Give the position of every Plasmodium parasite visible.
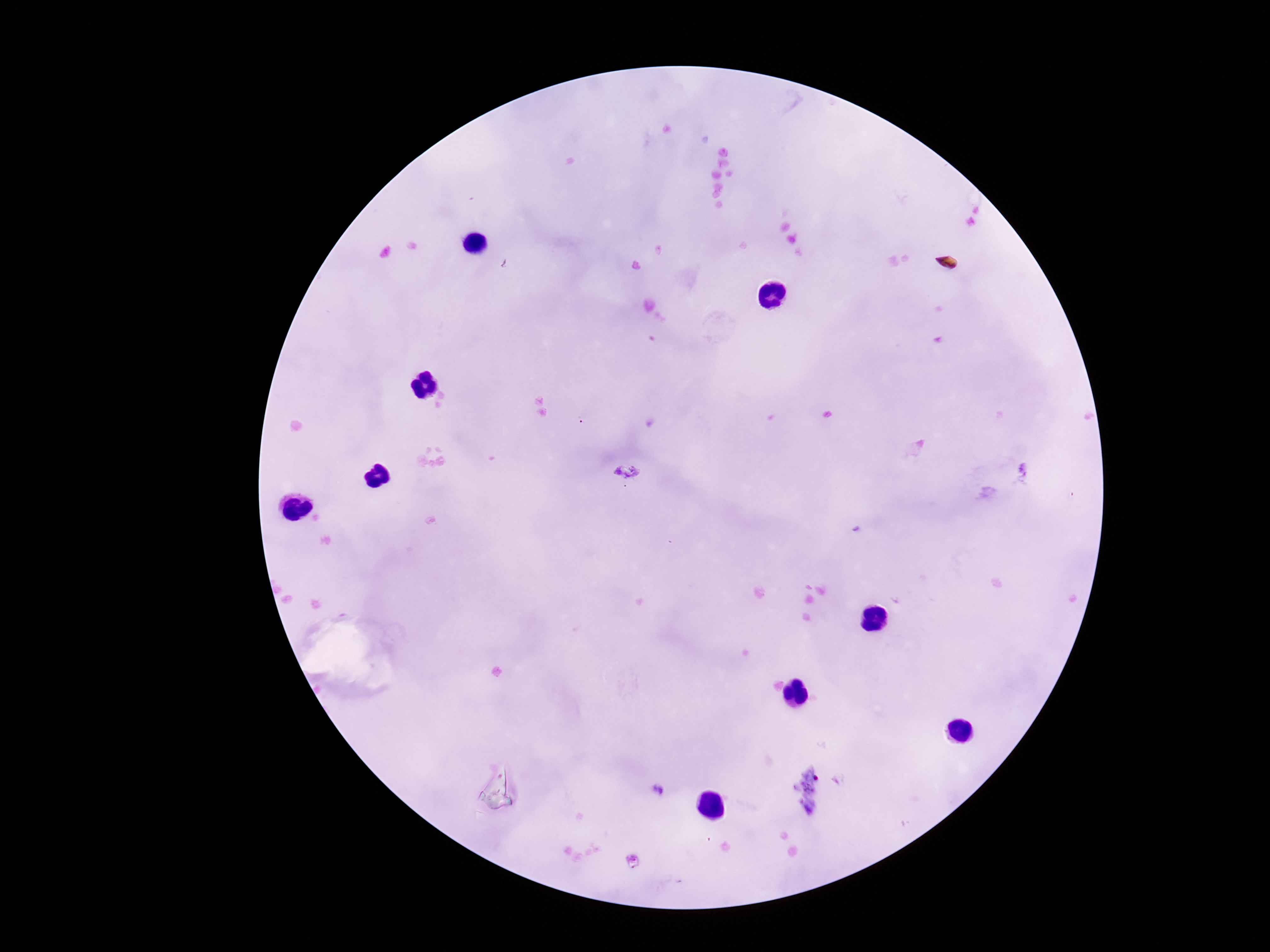

Approximate object centers, in pixels from the top-left corner.
Plasmodium parasites: (x=626, y=473), (x=661, y=791).

preparation = thick blood film
image size = 1270×952 pixels
field of view = single
magnification = 100x
stain = Giemsa
patient malaria status = infected
capture = smartphone camera through the microscope eyepiece